Locate every uninfected red blood cell.
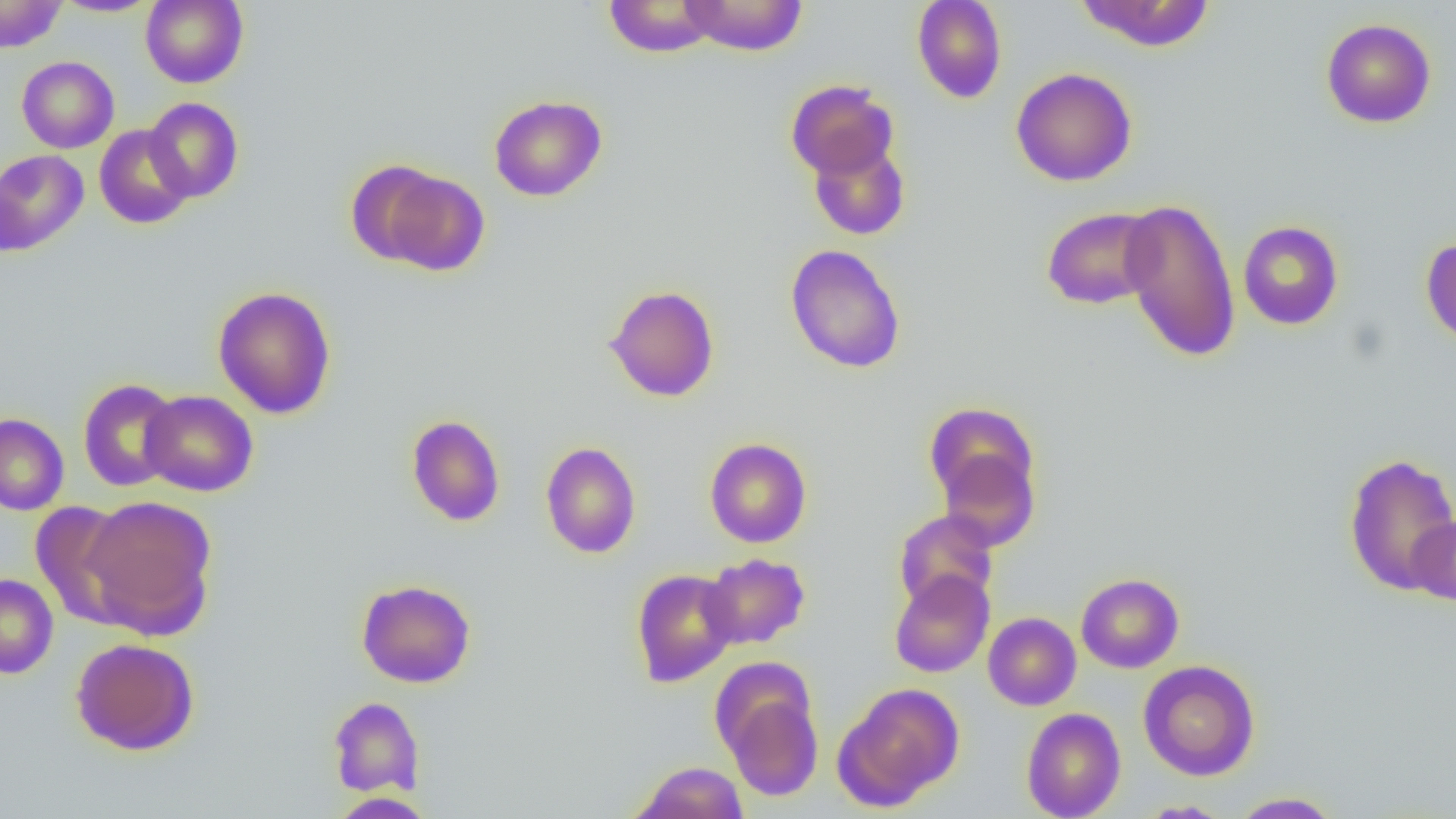
Approximate bounding boxes as (x1, y1, x2, y2) in pixels.
Uninfected red blood cells: (0, 0, 67, 53), (140, 0, 249, 88), (603, 0, 720, 57), (677, 0, 809, 56), (911, 0, 1007, 104), (52, 1, 161, 17), (1074, 1, 1217, 52), (1321, 18, 1436, 128), (16, 56, 119, 153), (1010, 67, 1138, 187), (785, 78, 898, 181), (488, 94, 607, 202), (144, 97, 244, 202), (94, 125, 194, 229), (807, 137, 911, 240), (0, 149, 89, 255), (345, 159, 447, 266), (374, 167, 491, 276), (1120, 197, 1241, 362), (1041, 206, 1162, 310), (1238, 220, 1344, 330), (1421, 237, 1456, 348), (785, 244, 906, 373), (604, 284, 720, 402), (212, 286, 337, 420), (77, 379, 181, 492), (140, 390, 258, 497), (923, 401, 1039, 512), (0, 413, 69, 515), (406, 414, 506, 527), (704, 438, 812, 548), (540, 441, 641, 558), (933, 443, 1042, 551), (1342, 452, 1456, 596), (81, 494, 217, 637), (30, 501, 140, 627), (893, 509, 998, 612), (1408, 514, 1456, 606), (700, 553, 810, 650), (630, 568, 740, 687), (890, 569, 995, 677), (1076, 572, 1184, 673), (0, 573, 59, 679), (356, 578, 476, 688), (983, 612, 1081, 710), (71, 637, 200, 756), (1138, 660, 1260, 781), (717, 678, 824, 803), (834, 682, 964, 810), (328, 696, 424, 797), (1021, 707, 1126, 819), (631, 761, 749, 819), (1229, 791, 1344, 818), (328, 792, 436, 818), (1137, 800, 1234, 818).

slide-level diagnosis = negative for blood parasites
field of view = one of a larger specimen
image size = 1456×819 pixels
magnification = 1000x
preparation = thin blood smear
modality = optical microscopy